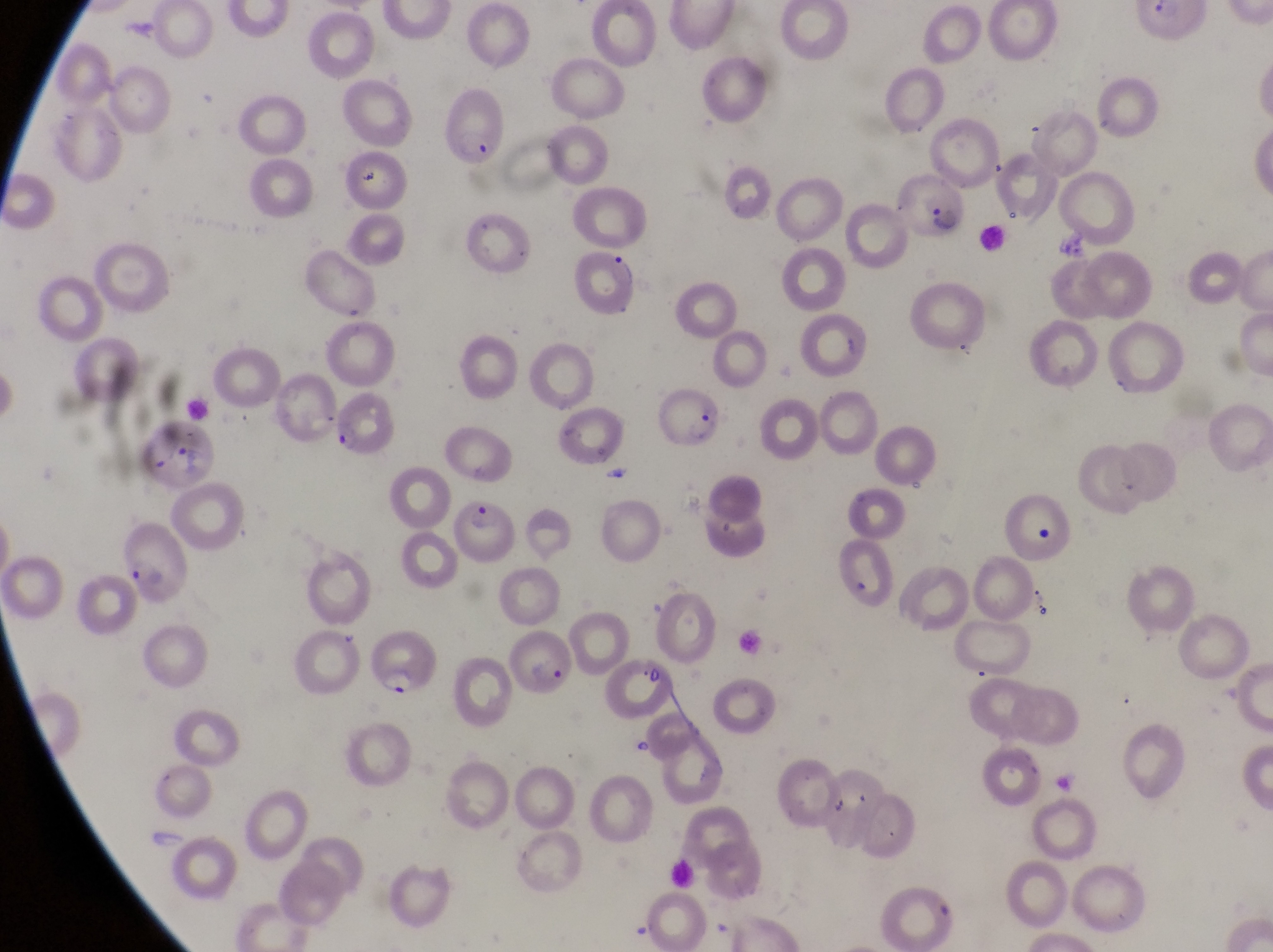
Approximate bounding boxes as {left, top, right, bottom} in pixels.
Summary:
  - Leukocyte locations: {981, 224, 1012, 262}, {1033, 524, 1061, 552}, {664, 856, 706, 895}
  - Parasitised red blood cell locations: {435, 90, 512, 167}, {896, 175, 968, 245}, {571, 248, 641, 310}, {652, 387, 726, 454}, {329, 395, 399, 460}, {127, 410, 214, 490}, {459, 495, 512, 567}, {115, 526, 192, 608}, {365, 626, 434, 704}
  - Artifact (platelet-like body, stain precipitate, or debris) locations: {361, 169, 380, 193}, {1055, 225, 1090, 264}, {599, 459, 638, 496}, {505, 631, 574, 696}, {632, 659, 665, 689}
  - Capture: smartphone photograph through the eyepiece of an Olympus CX-23 microscope
  - Image size: 1273×952 pixels
  - Preparation: thin blood smear
  - Country: Uganda
  - Magnification: 1000x
  - Field of view: single